Name the parasite shown.
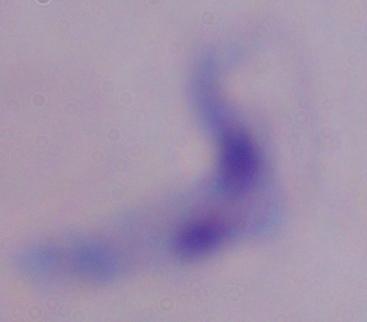
A trypanosome.

Micrograph. Captured at 1000x magnification.